State which parasite is depicted.
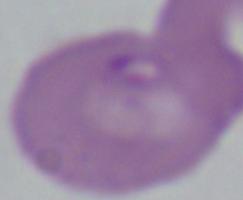

Babesia.

Summary:
  - Magnification: 1000x
  - Modality: photomicrograph